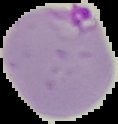
Result: malaria parasites identified. Image is 118×124 pixels. The area outside the segmented cell region is set to black. From a thin blood smear.